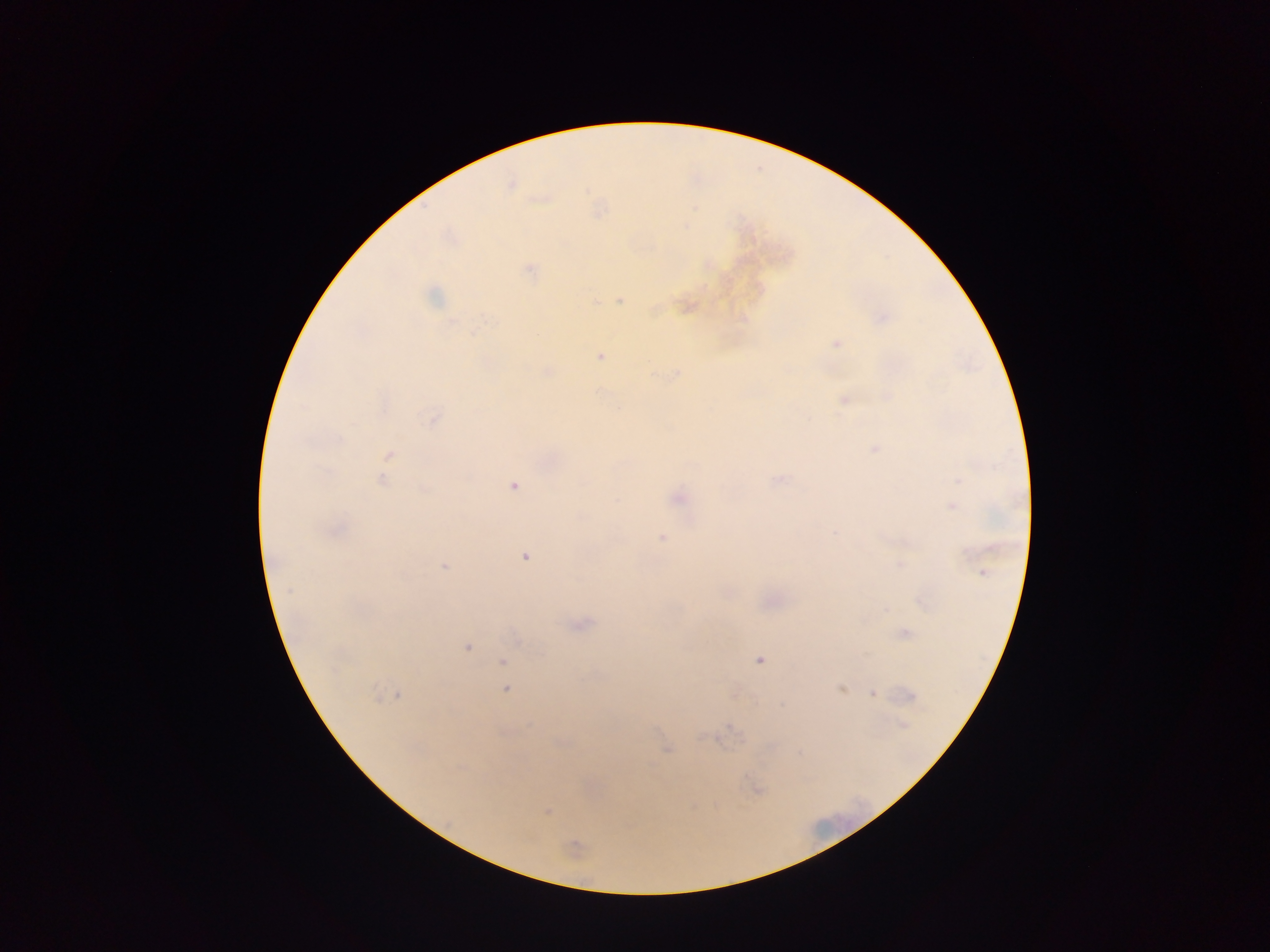

field of view = single
country = Ghana
image size = 1270×952 pixels
capture = mobile-phone photograph through a microscope
preparation = thick blood smear
Plasmodium parasite locations = approximate centers as (x, y) in pixels: (510, 184), (598, 210), (528, 270), (433, 296), (620, 299), (686, 307), (881, 318), (835, 344), (599, 356), (546, 371), (676, 374), (845, 400), (432, 417), (875, 448), (389, 455), (382, 480), (778, 480), (513, 485), (678, 497), (951, 504), (334, 530), (661, 536), (525, 556), (444, 565), (900, 565), (983, 573), (579, 625), (904, 632), (466, 646), (758, 660), (503, 662), (504, 677), (505, 689), (841, 689), (873, 693), (397, 694), (908, 695), (901, 724), (716, 738), (561, 742), (666, 749), (755, 789), (547, 810), (572, 849)